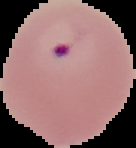

Summary:
  - Image type: segmented cell region with the area outside set to black
  - Preparation: thin blood film
  - Image size: 136×148 pixels
  - Malaria status: parasitized